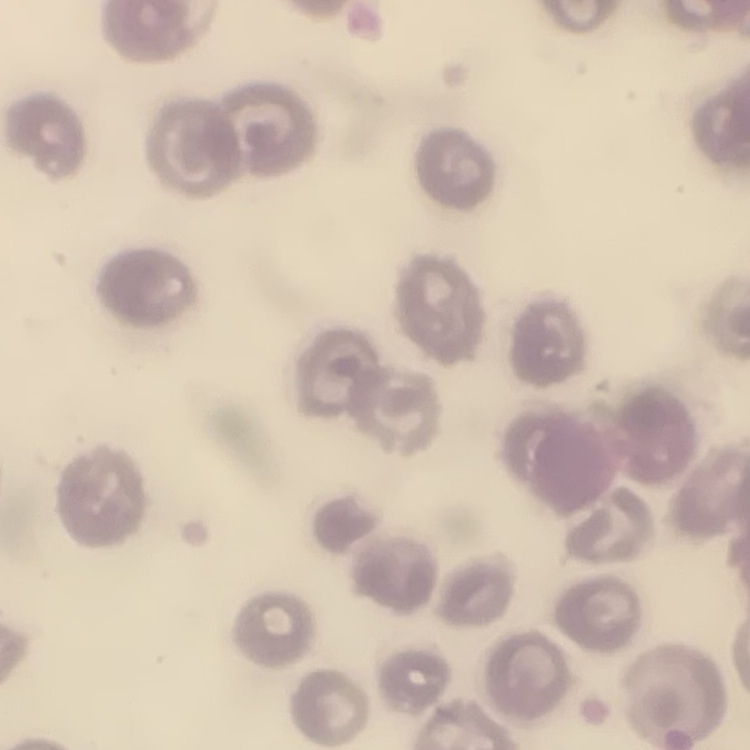

{
  "red_blood_cell_morphology": "no rouleaux formation",
  "stain": "Field's or Giemsa",
  "image_type": "one tile cut from a larger photomicrograph",
  "preparation": "thin peripheral smear"
}